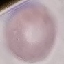
Malaria status: uninfected. Cell patch, automatically extracted from a larger field of view and resized to 64 × 64 pixels. Acquired by smartphone through the microscope eyepiece. Giemsa-stained preparation. Thin blood smear.